Classify this cell by malaria status.
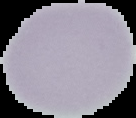
It is uninfected.

preparation: thin blood film
image_type: segmented cell region with the area outside set to black
image_size: 136×118 pixels